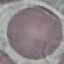
Malaria status: uninfected. Photographed with a smartphone camera at the microscope eyepiece. Thin blood smear. Giemsa stain. Automatically extracted cell patch, resized to 64 × 64 pixels.